Report the malaria status of this cell.
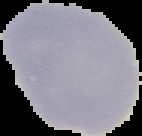

Uninfected.

image_size: 142×136 pixels
preparation: thin blood smear
image_type: segmented cell region with the area outside set to black